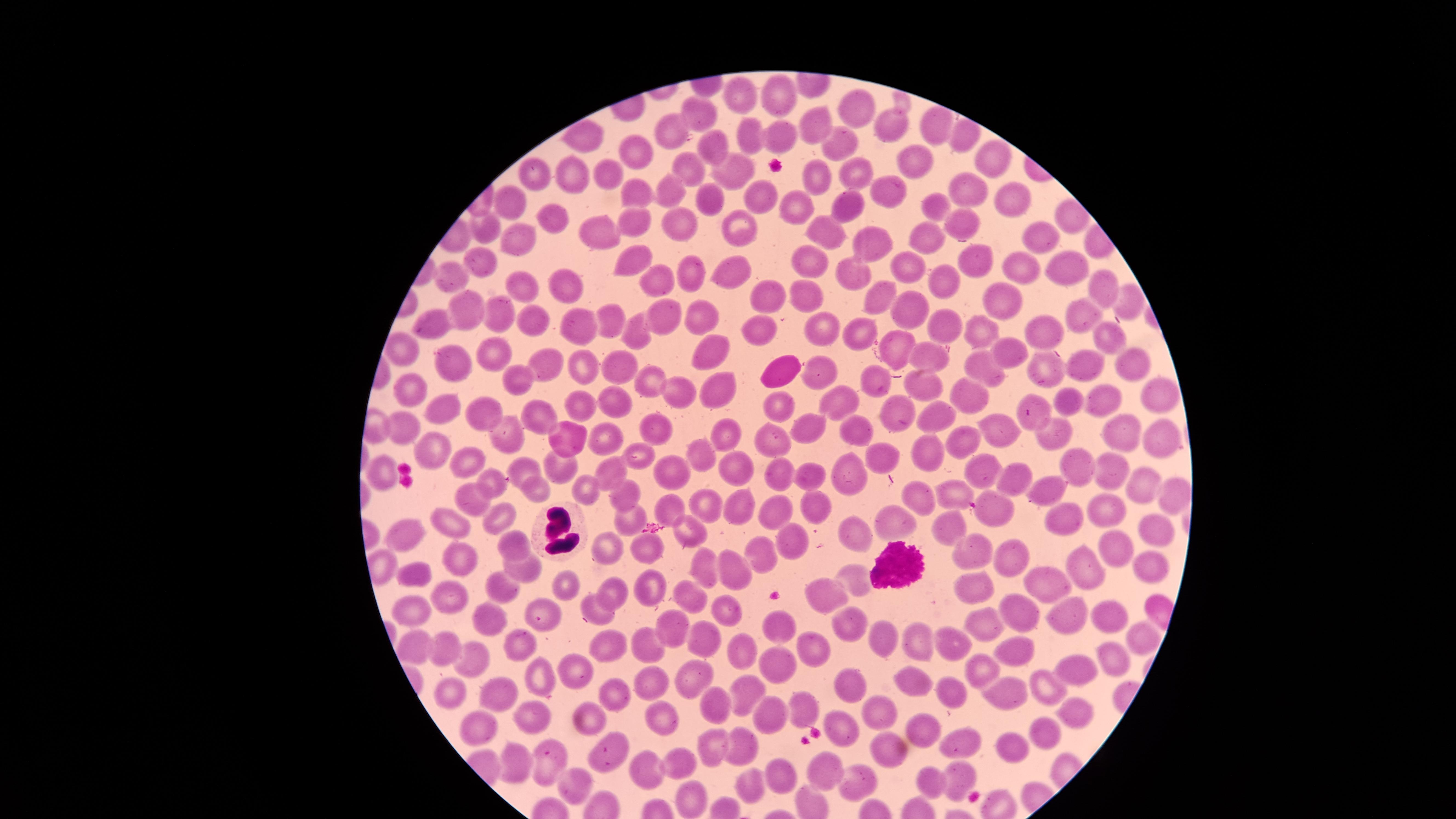

Approximate marker points, in pixels from the top-left corner. White blood cells: (x=778, y=373), (x=557, y=529), (x=897, y=564). Uninfected red blood cells: (x=783, y=91), (x=740, y=94), (x=854, y=108), (x=694, y=110), (x=813, y=126), (x=890, y=126), (x=671, y=128), (x=936, y=132), (x=780, y=134), (x=585, y=135), (x=750, y=136), (x=837, y=145), (x=714, y=146), (x=631, y=152), (x=913, y=159), (x=995, y=162), (x=852, y=166), (x=689, y=167), (x=738, y=169), (x=605, y=170), (x=528, y=174), (x=573, y=177), (x=815, y=182), (x=671, y=188), (x=882, y=190), (x=974, y=191), (x=631, y=196), (x=1010, y=196), (x=706, y=199), (x=762, y=199), (x=514, y=201), (x=796, y=206), (x=936, y=206), (x=847, y=210), (x=552, y=218), (x=962, y=222), (x=634, y=223), (x=828, y=228), (x=600, y=229), (x=681, y=229), (x=483, y=231), (x=742, y=234), (x=524, y=235), (x=932, y=235), (x=1039, y=236), (x=863, y=245), (x=630, y=256), (x=475, y=260), (x=970, y=264), (x=808, y=265), (x=1061, y=266), (x=452, y=271), (x=697, y=271), (x=732, y=271), (x=1022, y=271), (x=852, y=272), (x=911, y=273), (x=558, y=277), (x=659, y=282), (x=521, y=283), (x=939, y=285), (x=1106, y=294), (x=879, y=295), (x=767, y=298), (x=808, y=301), (x=1014, y=302), (x=465, y=310), (x=909, y=312), (x=499, y=314), (x=586, y=317), (x=667, y=317), (x=700, y=317), (x=530, y=318), (x=1082, y=318), (x=609, y=323), (x=436, y=325), (x=820, y=327), (x=857, y=329), (x=947, y=330), (x=981, y=331), (x=1045, y=332), (x=637, y=335), (x=761, y=335), (x=1111, y=338), (x=712, y=349), (x=892, y=349), (x=398, y=351), (x=493, y=351), (x=1010, y=352), (x=442, y=360), (x=545, y=360), (x=927, y=360), (x=1129, y=360), (x=622, y=366), (x=581, y=367), (x=1044, y=367), (x=1084, y=367), (x=824, y=371), (x=981, y=371), (x=515, y=376), (x=873, y=378), (x=651, y=383), (x=408, y=387), (x=1156, y=387), (x=716, y=390), (x=931, y=390), (x=679, y=394), (x=613, y=397), (x=834, y=398), (x=966, y=400), (x=1072, y=400), (x=1100, y=401), (x=585, y=402), (x=1035, y=404), (x=444, y=408), (x=781, y=410), (x=544, y=411), (x=936, y=413), (x=480, y=414), (x=899, y=416), (x=400, y=421), (x=655, y=423), (x=808, y=425), (x=1117, y=428), (x=999, y=429), (x=1053, y=430), (x=853, y=431), (x=726, y=432), (x=604, y=434), (x=511, y=435), (x=778, y=438), (x=1160, y=439), (x=561, y=441), (x=966, y=442), (x=433, y=446), (x=924, y=447), (x=701, y=448), (x=632, y=453), (x=882, y=459), (x=472, y=463), (x=560, y=464), (x=611, y=465), (x=1077, y=465), (x=980, y=466), (x=527, y=467), (x=738, y=468), (x=1107, y=471), (x=665, y=472), (x=783, y=472), (x=815, y=474), (x=379, y=475), (x=495, y=480), (x=851, y=480), (x=1020, y=481), (x=1143, y=483), (x=589, y=484), (x=960, y=491), (x=1051, y=492), (x=538, y=494), (x=629, y=494), (x=478, y=500), (x=706, y=502), (x=737, y=503), (x=918, y=504), (x=773, y=505), (x=671, y=507), (x=817, y=508), (x=1112, y=509), (x=445, y=511), (x=501, y=511), (x=996, y=513), (x=627, y=517), (x=1059, y=518), (x=899, y=525), (x=1156, y=525), (x=949, y=526), (x=693, y=529), (x=847, y=530), (x=411, y=534), (x=516, y=541), (x=599, y=544), (x=795, y=544), (x=648, y=547), (x=1107, y=549), (x=763, y=553), (x=975, y=559), (x=1015, y=559), (x=468, y=562), (x=712, y=565), (x=523, y=567), (x=1081, y=567), (x=1152, y=567), (x=739, y=571), (x=418, y=573), (x=852, y=578), (x=569, y=581), (x=501, y=584), (x=973, y=584), (x=1056, y=584), (x=652, y=588), (x=616, y=589), (x=824, y=594), (x=692, y=595), (x=450, y=598), (x=594, y=599), (x=1010, y=607), (x=409, y=613), (x=724, y=613), (x=1107, y=613), (x=546, y=616), (x=1076, y=616), (x=495, y=617), (x=985, y=624), (x=783, y=628), (x=676, y=629), (x=844, y=632), (x=707, y=633), (x=947, y=638), (x=1141, y=638), (x=882, y=639), (x=915, y=639), (x=423, y=644), (x=525, y=644), (x=653, y=645), (x=613, y=647), (x=738, y=648), (x=450, y=649), (x=1016, y=649), (x=809, y=651), (x=470, y=656), (x=1112, y=660), (x=779, y=664), (x=988, y=671), (x=1074, y=671), (x=696, y=672), (x=577, y=673), (x=914, y=676), (x=852, y=681), (x=546, y=682), (x=653, y=682), (x=999, y=685), (x=746, y=686), (x=621, y=690), (x=1045, y=690), (x=501, y=691), (x=946, y=693), (x=448, y=694), (x=720, y=702), (x=803, y=704), (x=1082, y=707), (x=874, y=709), (x=534, y=715), (x=771, y=715), (x=664, y=716), (x=591, y=719), (x=843, y=726), (x=477, y=727), (x=931, y=732), (x=1045, y=733), (x=966, y=737), (x=712, y=744), (x=741, y=745), (x=892, y=748), (x=1010, y=749), (x=609, y=751), (x=544, y=754), (x=688, y=758), (x=521, y=765), (x=650, y=766), (x=826, y=767), (x=960, y=774), (x=860, y=777), (x=784, y=778), (x=573, y=780), (x=747, y=780), (x=931, y=785), (x=696, y=798). Thin blood film. Single field of view. Giemsa stain. Smartphone photograph through the microscope eyepiece. The visible region is circular. Image is 1456×819 pixels. Presence: no malaria parasites detected.